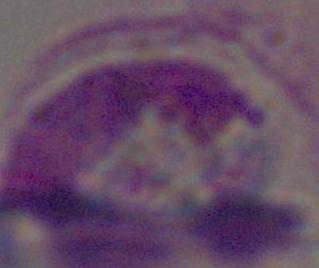
magnification: 1000x
modality: micrograph
identification: white blood cell